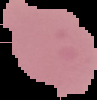

{
  "image_size": "97×100 pixels",
  "malaria_status": "uninfected",
  "image_type": "segmented cell region with the area outside set to black",
  "preparation": "thin blood film"
}